Name the parasite shown.
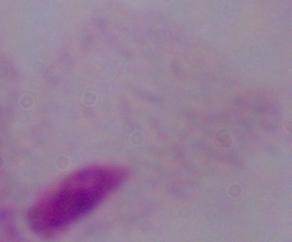
A trichomonad.

Summary:
  - Modality: micrograph
  - Magnification: 1000x